Outline each blood parasite and name the species.
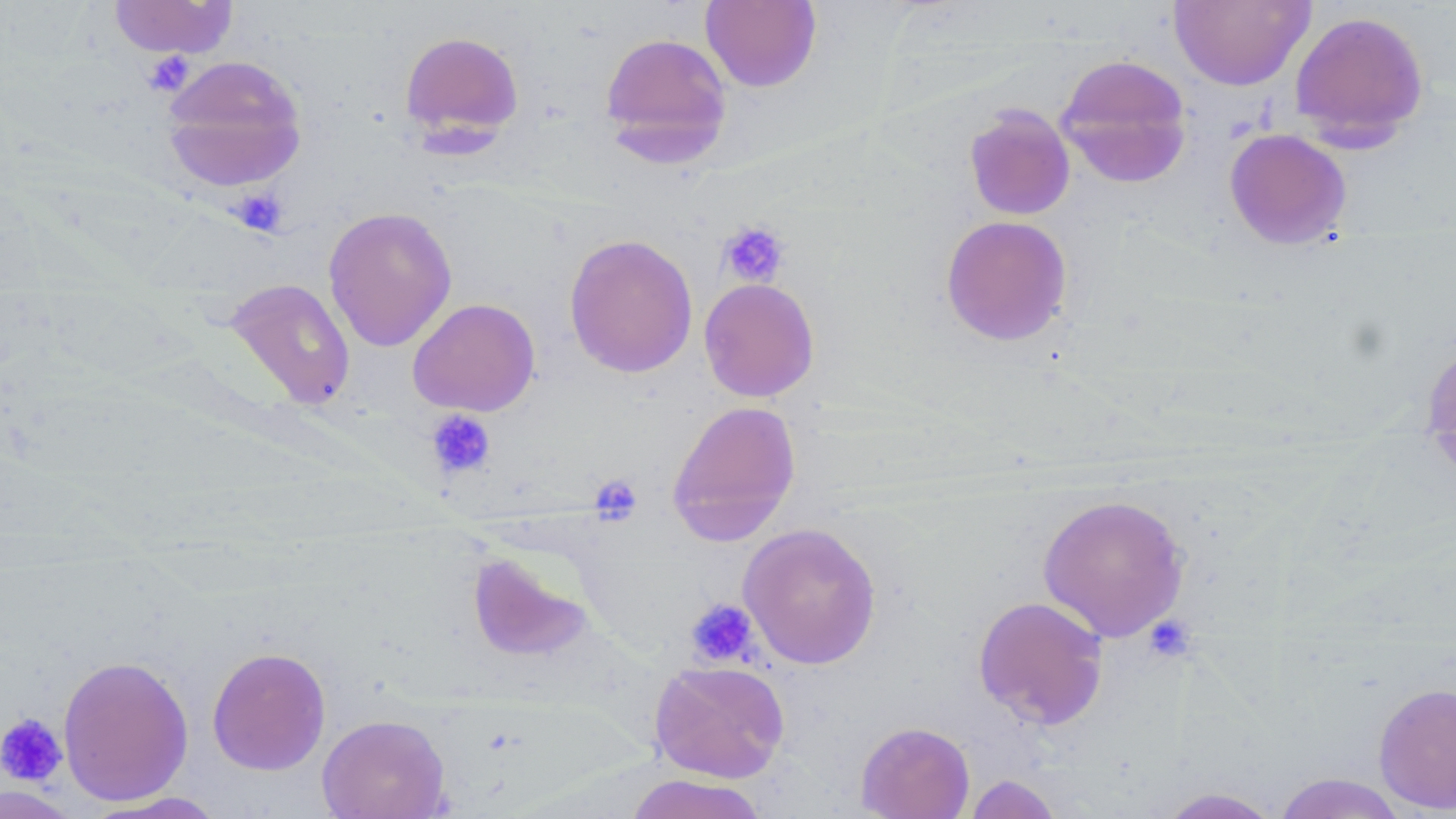
No blood parasites seen.

Approximate bounding boxes as named x1/y1/x2/y2 corners in pixels. Uninfected red blood cell locations: (x1=1169, y1=0, x2=1314, y2=91), (x1=107, y1=1, x2=239, y2=59), (x1=700, y1=1, x2=821, y2=93), (x1=1289, y1=10, x2=1429, y2=148), (x1=398, y1=29, x2=525, y2=145), (x1=599, y1=31, x2=733, y2=162), (x1=1055, y1=54, x2=1193, y2=189), (x1=161, y1=55, x2=308, y2=192), (x1=964, y1=105, x2=1075, y2=220), (x1=1224, y1=128, x2=1352, y2=249), (x1=323, y1=206, x2=457, y2=352), (x1=940, y1=214, x2=1073, y2=346), (x1=563, y1=233, x2=699, y2=379), (x1=222, y1=278, x2=357, y2=409), (x1=698, y1=278, x2=820, y2=402), (x1=407, y1=297, x2=540, y2=416), (x1=1419, y1=333, x2=1456, y2=484), (x1=666, y1=399, x2=802, y2=545), (x1=1037, y1=493, x2=1190, y2=642), (x1=737, y1=522, x2=882, y2=670), (x1=464, y1=547, x2=597, y2=665), (x1=972, y1=594, x2=1110, y2=731), (x1=206, y1=646, x2=331, y2=775), (x1=57, y1=654, x2=194, y2=806), (x1=649, y1=660, x2=790, y2=782), (x1=1373, y1=681, x2=1456, y2=815), (x1=316, y1=713, x2=451, y2=819), (x1=855, y1=721, x2=975, y2=819), (x1=1272, y1=772, x2=1409, y2=819), (x1=623, y1=774, x2=769, y2=819), (x1=963, y1=774, x2=1063, y2=818), (x1=0, y1=782, x2=83, y2=818), (x1=1154, y1=786, x2=1284, y2=818), (x1=83, y1=791, x2=230, y2=818). Platelet locations: (x1=142, y1=52, x2=196, y2=96), (x1=230, y1=188, x2=288, y2=236), (x1=717, y1=220, x2=791, y2=288), (x1=409, y1=298, x2=541, y2=422), (x1=426, y1=410, x2=495, y2=478), (x1=589, y1=474, x2=643, y2=525), (x1=685, y1=599, x2=760, y2=668), (x1=1142, y1=615, x2=1197, y2=663), (x1=0, y1=712, x2=68, y2=786). Slide-level diagnosis: negative for blood parasites. Optical microscopy. Single field of view. Thin blood smear. May-Grünwald-Giemsa stain. Image is 1456×819 pixels. 1000x magnification.